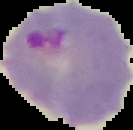

preparation = thin blood smear
image type = cell region segmented out of the field of view; surrounding area masked to black
image size = 133×130 pixels
malaria status = parasitized